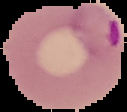
Summary:
  - Image size: 127×112 pixels
  - Image type: cell region segmented out of the field of view; surrounding area masked to black
  - Preparation: thin blood smear
  - Result: Plasmodium parasites identified